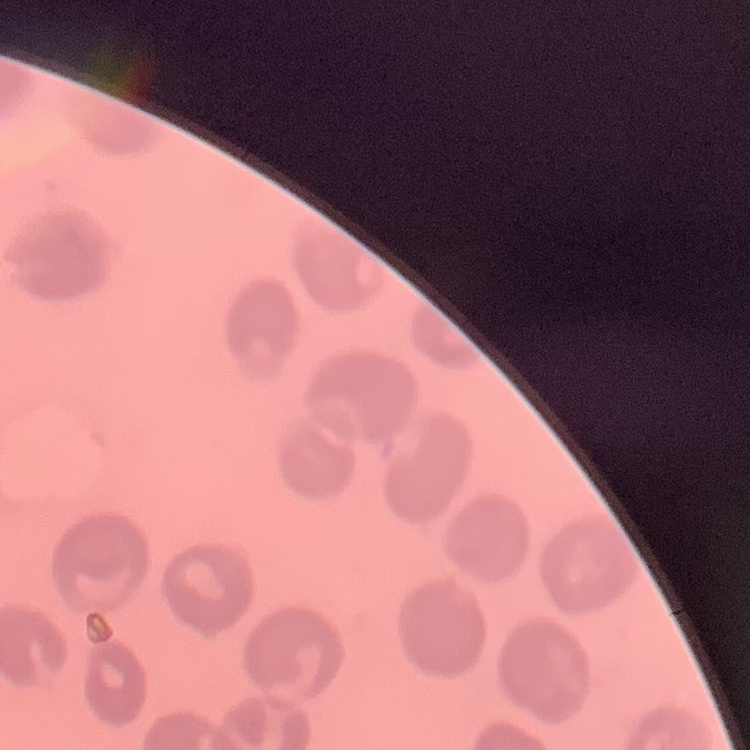

{
  "erythrocyte_morphology": "no rouleaux formation",
  "image_type": "one tile cut from a larger photomicrograph",
  "stain": "Field's or Giemsa",
  "preparation": "thin blood smear"
}